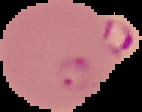

image_type: segmented cell region with the area outside set to black
malaria_status: parasitized
preparation: thin blood film
image_size: 142×112 pixels